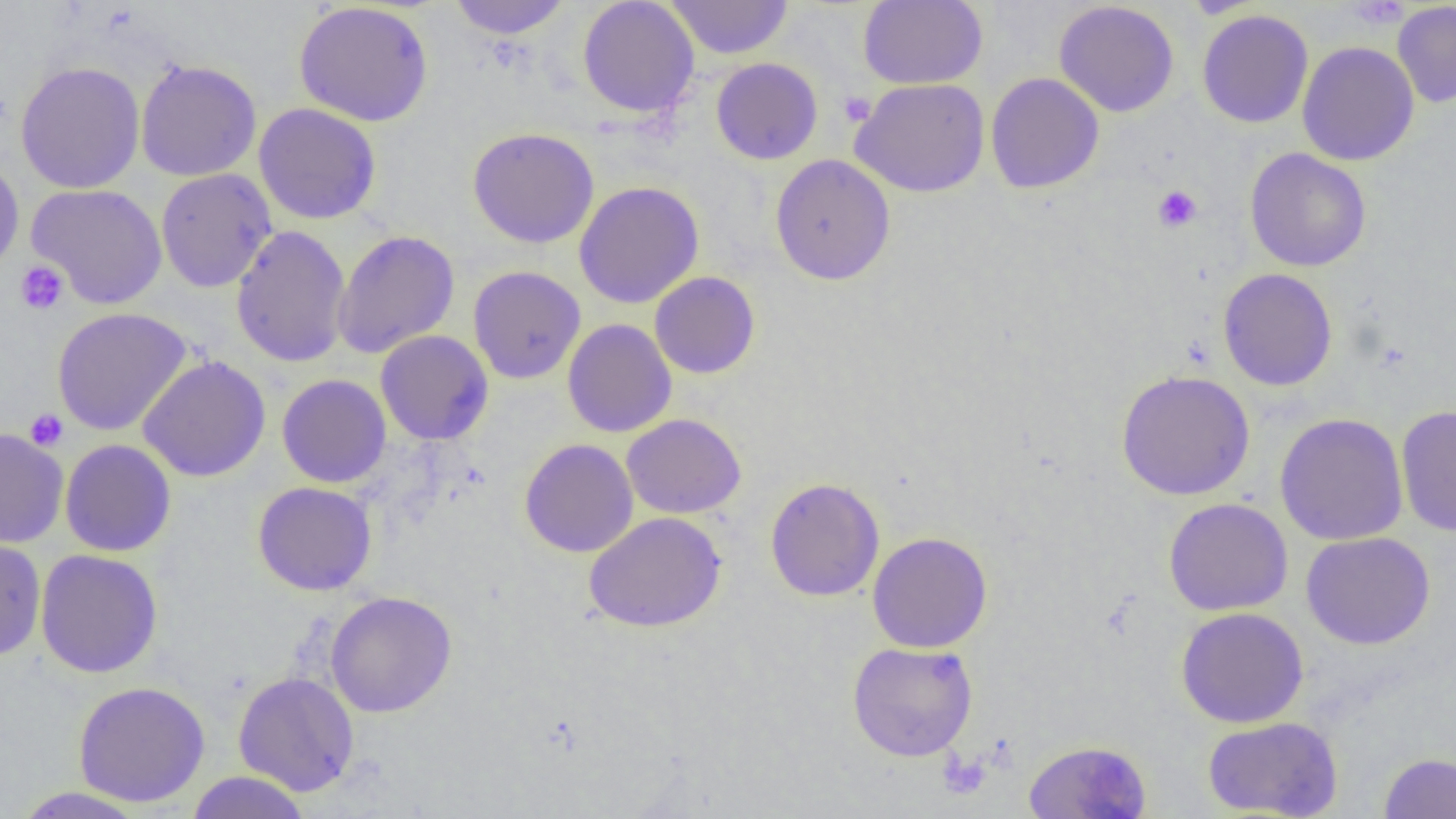

Approximate bounding boxes as (x1, y1, x2, y2) in pixels. Uninfected red blood cell locations: (447, 0, 571, 40), (577, 0, 700, 118), (665, 0, 793, 59), (858, 0, 988, 89), (294, 1, 434, 126), (1054, 1, 1180, 118), (1392, 2, 1456, 108), (1196, 9, 1313, 129), (1297, 41, 1419, 166), (711, 58, 823, 165), (136, 59, 262, 181), (15, 61, 145, 194), (986, 72, 1104, 194), (850, 78, 990, 197), (253, 103, 382, 225), (467, 127, 599, 249), (1245, 147, 1371, 272), (770, 154, 896, 285), (0, 156, 25, 277), (155, 168, 277, 293), (574, 181, 705, 309), (27, 183, 167, 309), (230, 225, 352, 367), (332, 230, 460, 359), (467, 265, 586, 384), (1218, 268, 1338, 391), (649, 271, 760, 379), (52, 307, 192, 436), (562, 319, 677, 437), (375, 329, 493, 445), (137, 356, 271, 482), (1115, 370, 1255, 500), (277, 374, 391, 488), (1396, 404, 1456, 536), (1274, 412, 1409, 546), (622, 413, 746, 519), (0, 427, 68, 548), (60, 439, 176, 557), (520, 439, 639, 558), (765, 477, 885, 602), (252, 482, 377, 595), (1163, 498, 1293, 616), (584, 511, 726, 633), (867, 531, 993, 653), (1301, 531, 1436, 650), (0, 537, 47, 661), (35, 549, 163, 678), (325, 591, 457, 717), (1175, 606, 1309, 728), (847, 641, 978, 761), (233, 671, 359, 796), (73, 681, 210, 807), (1202, 716, 1343, 818), (1023, 739, 1153, 818), (1379, 752, 1456, 818), (185, 771, 312, 819), (10, 786, 149, 818). Platelet locations: (1348, 0, 1409, 30), (839, 91, 876, 127), (1152, 185, 1202, 233), (15, 261, 69, 315), (24, 409, 68, 451), (939, 751, 991, 799). Slide-level diagnosis: negative for blood parasites. Light microscopy. Image is 1456×819 pixels. Thin blood film. Captured at 1000x magnification. Single field of view.